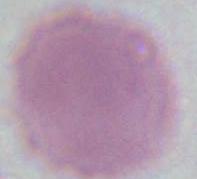
Summary:
  - Modality: micrograph
  - Magnification: 1000x
  - Identification: erythrocyte